Point out each malaria parasite.
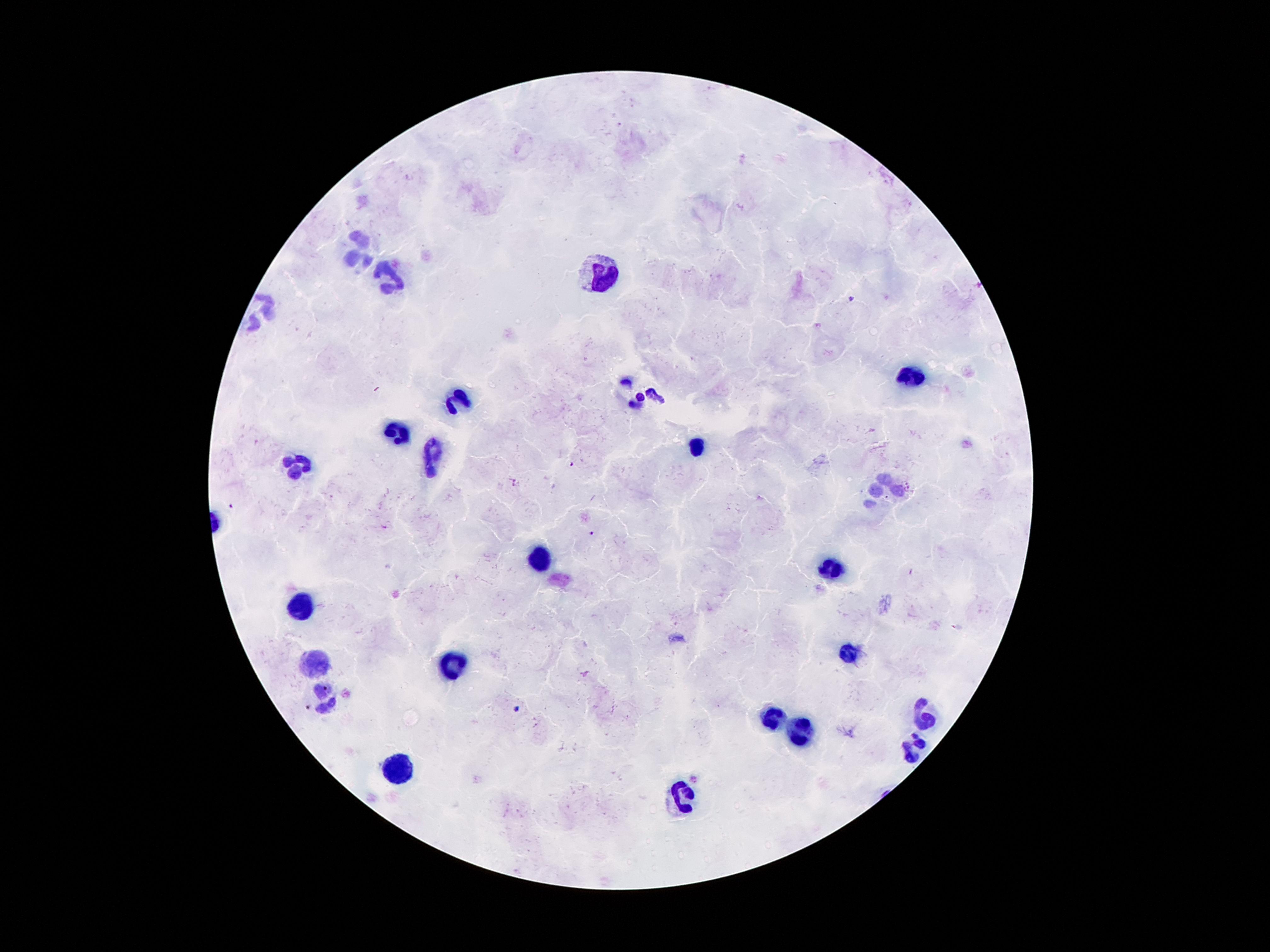
Approximate centers as {x, y} in pixels.
Malaria parasites: {850, 300}, {571, 466}, {516, 482}, {231, 506}, {593, 533}, {516, 709}, {695, 780}.

Leukocyte locations: {355, 253}, {598, 273}, {386, 278}, {910, 376}, {641, 397}, {458, 399}, {388, 431}, {700, 446}, {431, 460}, {298, 462}, {882, 489}, {542, 558}, {830, 570}, {307, 609}, {848, 654}, {455, 662}, {315, 665}, {322, 698}, {926, 717}, {770, 720}, {798, 733}, {914, 749}, {402, 774}, {680, 798}. Patient malaria status: positive for Plasmodium falciparum. Giemsa stain. One field from this slide. Thick peripheral-blood smear. 100x magnification. Image is 1270×952 pixels. Photographed through the microscope eyepiece with a smartphone camera.